Outline each blood parasite and name the species.
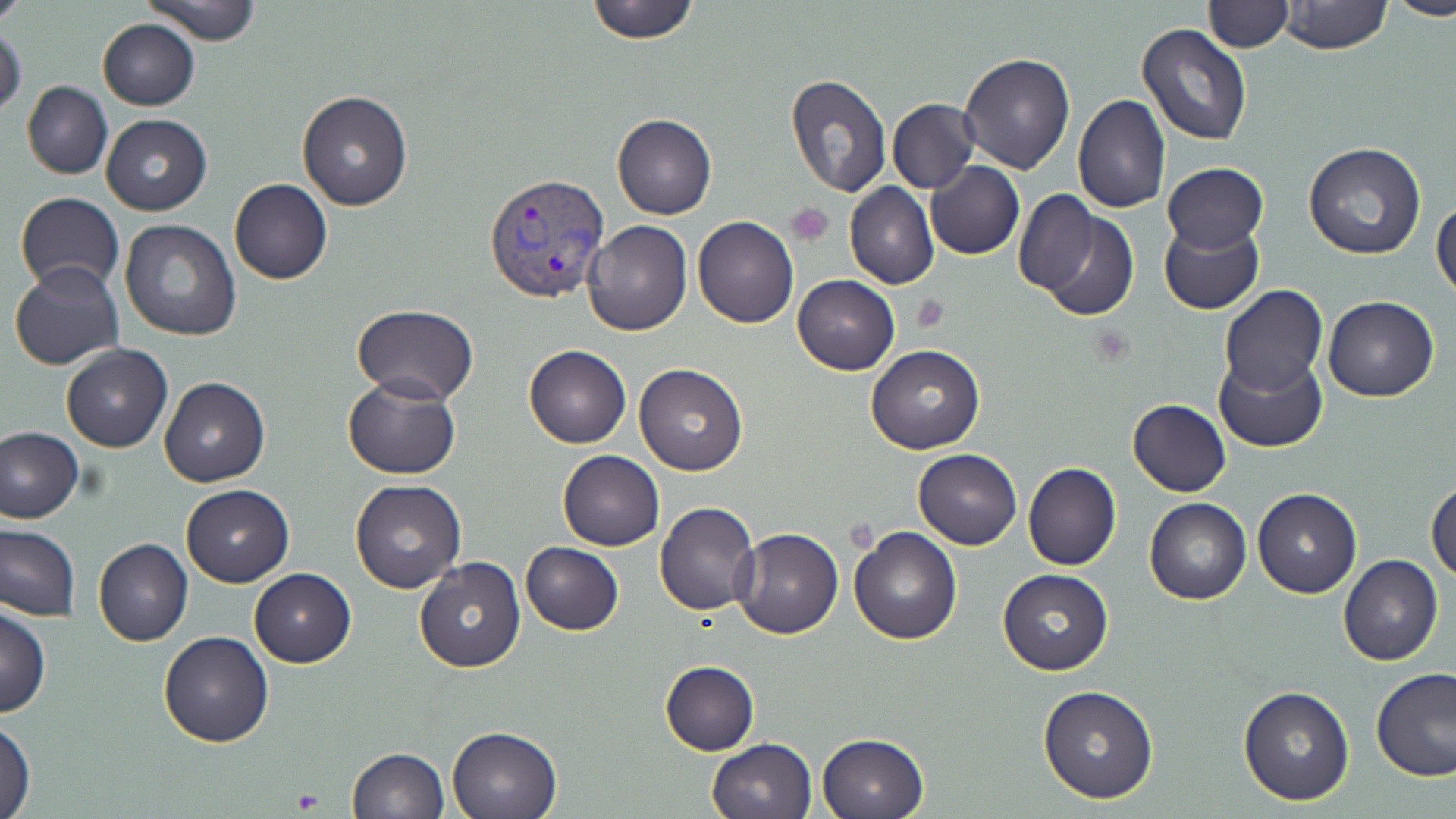

Approximate bounding boxes as [x1, y1, x2, y2] in pixels.
Plasmodium vivax-infected red blood cells: [483, 172, 610, 304].
No Plasmodium falciparum, Plasmodium ovale, Plasmodium malariae, Babesia divergens, or Trypanosoma brucei observed.

Summary:
  - Uninfected red blood cell locations: [0, 0, 28, 26], [141, 0, 262, 45], [582, 0, 701, 45], [1279, 0, 1393, 55], [1385, 0, 1456, 20], [1203, 1, 1292, 52], [97, 18, 199, 110], [1136, 24, 1253, 149], [0, 26, 26, 118], [958, 54, 1075, 175], [786, 73, 891, 197], [22, 81, 113, 179], [297, 90, 413, 211], [1073, 94, 1170, 214], [888, 98, 980, 194], [100, 112, 212, 215], [611, 113, 717, 220], [1303, 142, 1427, 260], [926, 161, 1024, 259], [1162, 162, 1267, 254], [230, 179, 332, 286], [845, 182, 938, 289], [1013, 188, 1099, 296], [15, 193, 124, 292], [1432, 197, 1456, 303], [1026, 202, 1142, 321], [692, 216, 799, 327], [119, 219, 240, 340], [1159, 219, 1264, 315], [583, 220, 692, 335], [9, 262, 125, 370], [793, 275, 899, 375], [1220, 284, 1328, 396], [1322, 296, 1440, 402], [352, 304, 478, 403], [61, 344, 172, 452], [524, 345, 631, 448], [867, 345, 983, 453], [1213, 351, 1327, 453], [634, 363, 747, 475], [343, 377, 462, 479], [159, 378, 270, 486], [1128, 398, 1232, 496], [0, 428, 83, 522], [558, 449, 665, 552], [914, 449, 1021, 549], [1022, 463, 1121, 571], [350, 479, 465, 593], [1426, 479, 1456, 583], [181, 484, 293, 586], [1253, 488, 1361, 597], [1145, 498, 1251, 604], [654, 501, 759, 616], [0, 522, 80, 620], [849, 525, 961, 644], [731, 529, 844, 640], [94, 538, 192, 646], [520, 541, 622, 635], [1339, 555, 1442, 666], [414, 556, 525, 672], [249, 568, 356, 668], [997, 569, 1112, 674], [0, 605, 51, 718], [157, 631, 274, 748], [659, 660, 760, 755], [1371, 668, 1456, 782], [1037, 683, 1160, 804], [1237, 684, 1355, 805], [0, 719, 36, 818], [446, 724, 563, 819], [816, 732, 929, 819], [706, 738, 816, 819], [346, 748, 448, 819]
  - Platelet locations: [787, 203, 832, 245], [911, 296, 950, 332], [290, 788, 322, 812]
  - Slide-level diagnosis: Plasmodium vivax
  - Field of view: one of a larger specimen
  - Magnification: 1000x
  - Modality: light microscopy
  - Image size: 1456×819 pixels
  - Preparation: thin blood smear
  - Stain: May-Grünwald-Giemsa